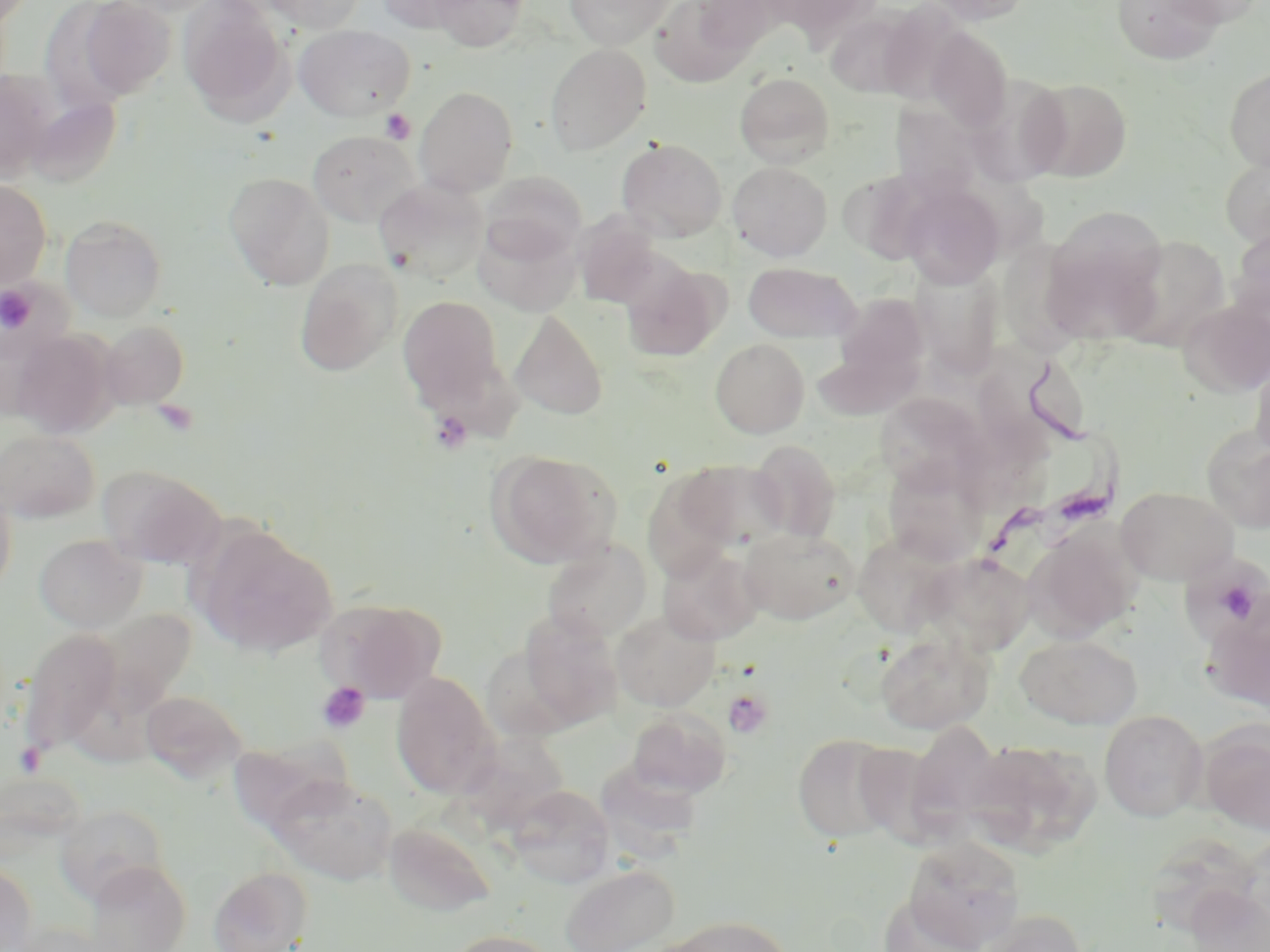
Summary:
  - Coordinate format: approximate bounding boxes as [x1, y1, x2, y2] in pixels
  - Trypanosoma brucei locations: [976, 358, 1123, 570]
  - Uninfected red blood cell locations: [70, 0, 178, 102], [178, 0, 293, 122], [260, 0, 367, 33], [374, 0, 479, 32], [429, 0, 530, 52], [564, 0, 675, 49], [649, 0, 756, 87], [689, 0, 785, 56], [761, 0, 882, 44], [918, 0, 1036, 26], [1111, 0, 1228, 65], [1161, 0, 1265, 27], [824, 7, 921, 99], [293, 24, 416, 121], [924, 25, 1014, 133], [544, 44, 651, 155], [1224, 66, 1270, 172], [0, 72, 56, 182], [734, 72, 834, 167], [967, 75, 1071, 189], [1025, 77, 1134, 182], [414, 86, 519, 196], [23, 95, 122, 188], [891, 106, 981, 198], [307, 130, 420, 228], [616, 138, 727, 242], [1220, 153, 1270, 250], [727, 161, 832, 261], [478, 170, 588, 263], [224, 171, 336, 290], [373, 178, 488, 284], [0, 180, 51, 289], [898, 182, 1005, 288], [1040, 210, 1173, 342], [572, 213, 663, 307], [60, 214, 168, 323], [474, 215, 582, 316], [1229, 226, 1270, 322], [1110, 234, 1232, 351], [295, 258, 404, 376], [619, 259, 727, 362], [744, 262, 861, 343], [911, 263, 1005, 380], [831, 291, 930, 393], [398, 296, 504, 407], [1178, 299, 1270, 397], [510, 310, 609, 420], [99, 320, 190, 409], [11, 329, 119, 438], [710, 338, 810, 437], [999, 347, 1094, 453], [1250, 354, 1270, 459], [875, 392, 986, 494], [968, 425, 1062, 513], [1202, 426, 1270, 532], [0, 428, 100, 523], [748, 440, 841, 544], [488, 450, 622, 568], [881, 458, 990, 566], [678, 459, 791, 550], [96, 464, 227, 570], [643, 472, 744, 578], [0, 483, 17, 599], [1117, 486, 1237, 585], [1025, 521, 1142, 640], [195, 527, 337, 657], [738, 527, 860, 625], [850, 532, 962, 637], [34, 533, 146, 632], [541, 539, 653, 641], [657, 546, 764, 645], [920, 551, 1037, 656], [317, 597, 445, 702], [1202, 601, 1270, 714], [92, 608, 197, 722], [612, 608, 720, 711], [517, 611, 624, 728], [19, 627, 122, 753], [875, 631, 994, 735], [1015, 634, 1142, 729], [480, 644, 579, 742], [391, 672, 500, 799], [140, 689, 248, 783], [626, 707, 732, 798], [1099, 709, 1208, 821], [906, 721, 1003, 829], [1199, 721, 1270, 834], [792, 733, 900, 843], [974, 735, 1105, 860], [596, 760, 700, 857], [268, 774, 398, 885], [507, 785, 615, 887], [53, 804, 170, 904], [383, 821, 496, 918], [902, 836, 1025, 952], [0, 860, 38, 952], [83, 860, 192, 952], [560, 863, 680, 952], [208, 866, 314, 952], [1181, 881, 1270, 952], [878, 893, 984, 952], [977, 909, 1091, 952], [664, 915, 795, 952], [443, 929, 560, 952]
  - Platelet locations: [380, 109, 415, 144], [0, 285, 38, 335], [154, 399, 198, 436], [429, 410, 473, 454], [1206, 572, 1265, 630], [316, 682, 371, 734], [723, 689, 774, 739], [15, 741, 47, 778]
  - Slide-level diagnosis: Trypanosoma brucei
  - Preparation: thin blood film
  - Field of view: single
  - Image size: 1270×952 pixels
  - Modality: light microscopy
  - Magnification: 1000x
  - Stain: May-Grünwald-Giemsa